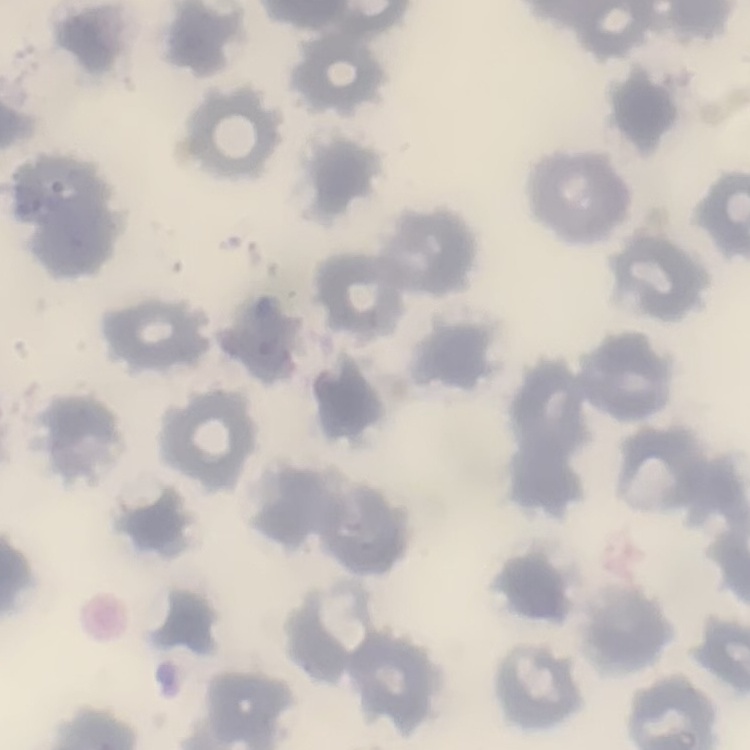

{
  "red_blood_cell_morphology": "no rouleaux formation",
  "image_type": "one tile cut from a larger photomicrograph",
  "stain": "Field's or Giemsa",
  "preparation": "thin blood film"
}